Assess the morphology of the erythrocytes.
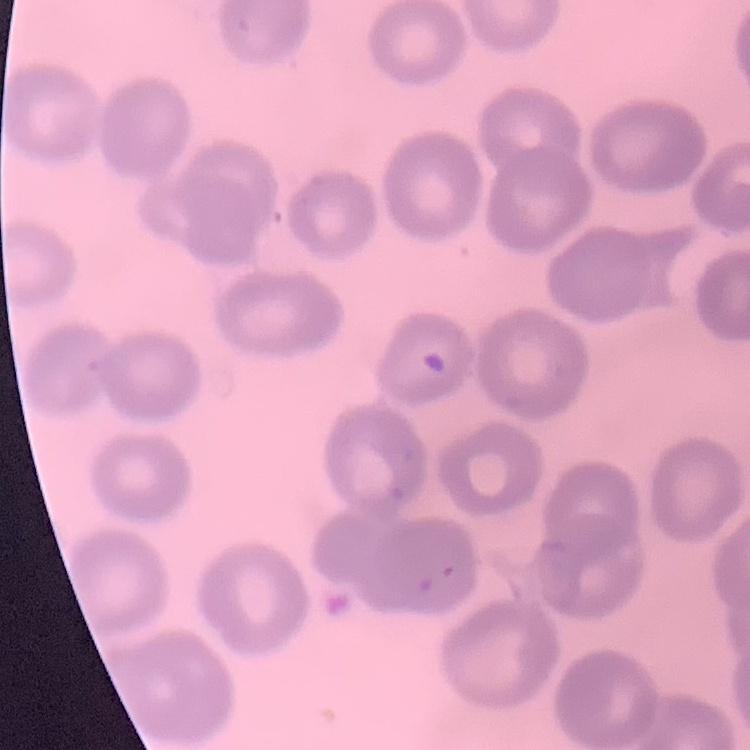

They show no rouleaux formation.

image type = one tile cut from a larger photomicrograph
preparation = thin peripheral smear
stain = Field's or Giemsa